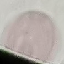
result: no malaria parasites detected
preparation: thin smear
capture: smartphone camera at the microscope eyepiece
stain: Giemsa
image_type: cell patch, automatically extracted from a larger field of view and resized to 64 × 64 pixels